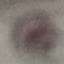

Summary:
  - Malaria status: uninfected
  - Stain: Giemsa
  - Preparation: thin smear
  - Image type: automatically extracted cell patch, resized to 64 × 64 pixels
  - Capture: smartphone camera at the microscope eyepiece